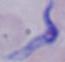 A trypanosome is shown. Micrograph. Captured at 1000x magnification.